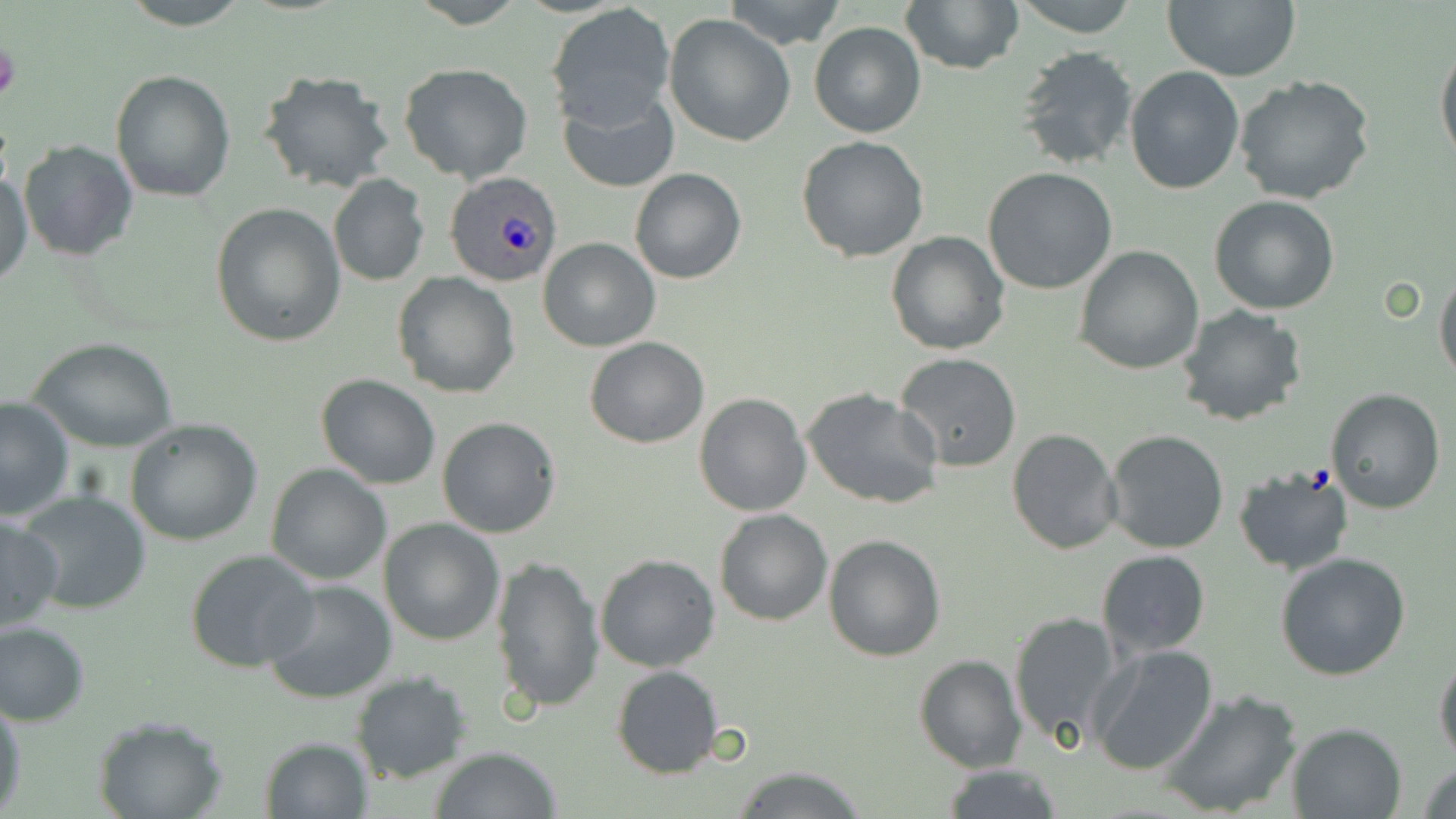
Summary:
  - Coordinate format: approximate bounding boxes as (x1,y1)-(x2,y2) corner pairs in pixels
  - Platelet locations: (0,40)-(21,105)
  - Plasmodium ovale-infected red blood cell locations: (444,170)-(563,287)
  - Uninfected red blood cell locations: (116,0)-(254,29), (721,0)-(849,50), (899,0)-(1022,74), (1014,0)-(1139,37), (1160,0)-(1301,82), (546,4)-(675,129), (663,14)-(796,147), (808,21)-(926,138), (1435,37)-(1456,170), (1015,46)-(1141,172), (398,62)-(533,183), (1124,66)-(1246,194), (110,69)-(237,202), (257,69)-(395,194), (1234,76)-(1377,207), (558,90)-(679,194), (796,135)-(931,261), (18,140)-(139,262), (628,167)-(746,284), (0,168)-(32,289), (982,168)-(1118,295), (328,175)-(429,286), (1209,195)-(1340,315), (211,203)-(345,346), (380,225)-(500,367), (886,231)-(1010,355), (539,237)-(660,352), (1073,244)-(1203,374), (1435,266)-(1456,385), (392,273)-(520,398), (1176,306)-(1309,427), (28,336)-(180,453), (585,337)-(710,448), (894,353)-(1023,473), (315,374)-(442,490), (801,386)-(944,510), (1324,388)-(1446,513), (693,391)-(812,516), (0,397)-(74,520), (436,416)-(561,538), (124,417)-(263,546), (1007,428)-(1120,554), (1103,429)-(1230,554), (266,463)-(392,585), (1233,465)-(1355,575), (17,489)-(151,616), (714,509)-(833,626), (0,515)-(66,632), (378,518)-(505,645), (823,533)-(946,661), (1096,548)-(1211,657), (184,549)-(320,673), (595,553)-(721,672), (1275,553)-(1411,682), (490,555)-(605,717), (262,579)-(399,704), (1008,610)-(1123,748), (0,620)-(91,727), (1088,644)-(1219,775), (914,654)-(1025,772), (1434,654)-(1456,766), (611,665)-(724,779), (349,671)-(473,784), (1157,688)-(1302,818), (0,695)-(24,815), (94,715)-(228,819), (1285,722)-(1408,818), (258,736)-(372,817), (431,744)-(563,818), (1418,761)-(1456,819), (939,763)-(1063,819), (731,766)-(869,819)
  - Slide-level diagnosis: Plasmodium ovale
  - Image size: 1456×819 pixels
  - Stain: May-Grünwald-Giemsa
  - Modality: light microscopy
  - Magnification: 1000x
  - Preparation: thin blood film
  - Field of view: one of a larger specimen